Name the cell type shown.
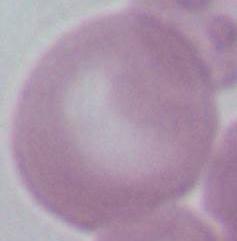
This is an erythrocyte.

{
  "magnification": "1000x",
  "modality": "photomicrograph"
}